Give the location of every parasitized red blood cell.
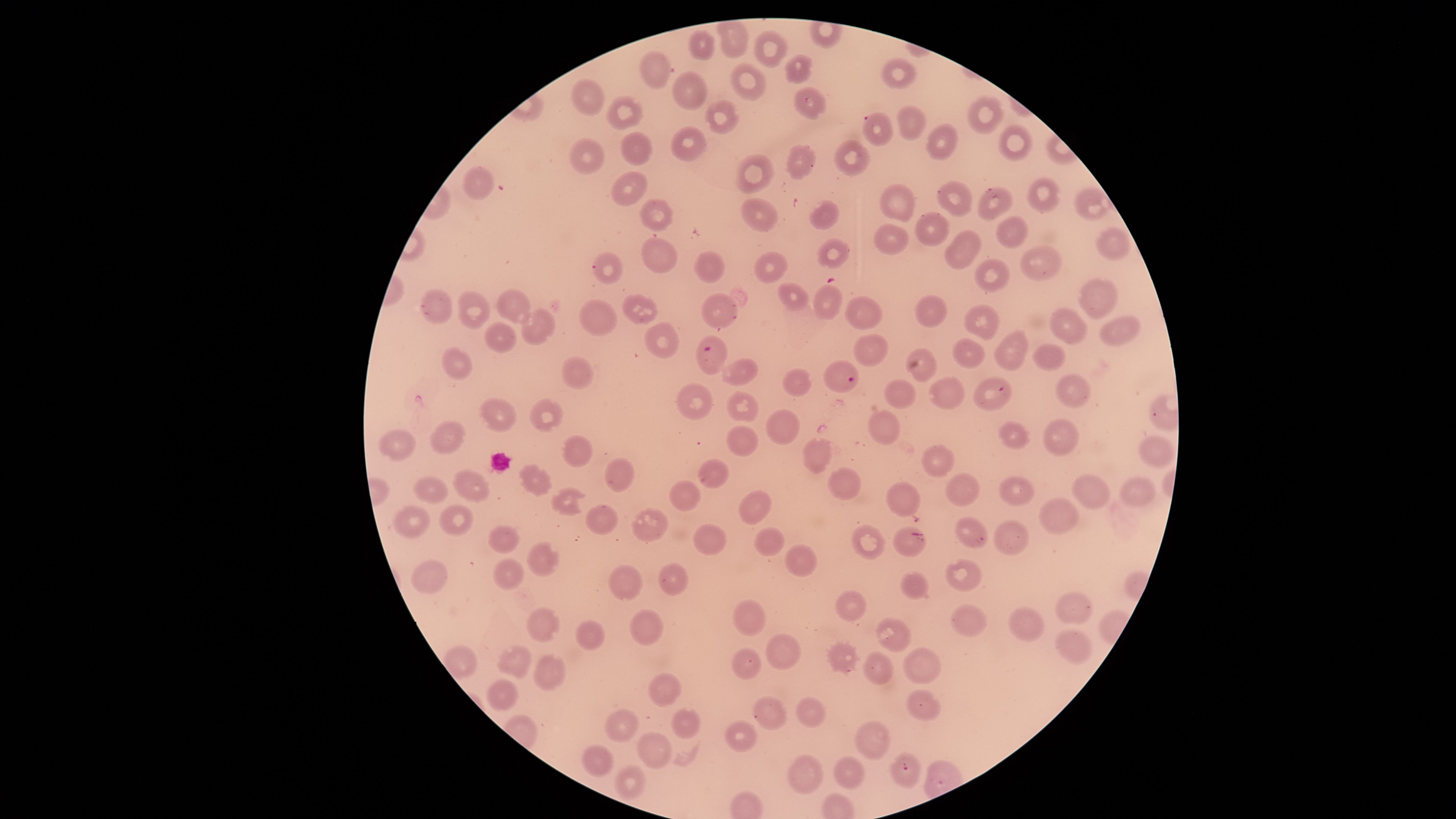
Approximate bounding boxes as (left, top, right, bottom) in pixels.
Parasitized red blood cells: (695, 335, 727, 375), (823, 360, 859, 393).

Approximate bounding boxes as (left, top, right, bottom) in pixels. Uninfected red blood cells: (718, 20, 749, 58), (688, 29, 715, 60), (754, 29, 787, 68), (640, 50, 670, 90), (784, 53, 813, 84), (880, 58, 917, 89), (730, 62, 766, 100), (672, 70, 705, 110), (571, 79, 605, 116), (793, 86, 826, 119), (607, 95, 642, 130), (967, 95, 1004, 134), (706, 99, 739, 135), (895, 105, 926, 140), (863, 111, 893, 145), (928, 123, 959, 160), (999, 124, 1033, 161), (671, 126, 706, 161), (621, 131, 652, 166), (568, 137, 604, 175), (834, 140, 870, 176), (788, 144, 816, 179), (737, 154, 775, 194), (463, 166, 494, 199), (612, 171, 647, 205), (1028, 177, 1059, 213), (938, 180, 972, 216), (880, 184, 915, 224), (978, 187, 1013, 220), (1075, 188, 1111, 221), (739, 197, 779, 232), (639, 198, 673, 232), (810, 200, 839, 229), (915, 211, 949, 246), (996, 216, 1029, 247), (873, 223, 909, 255), (1095, 227, 1130, 260), (944, 229, 983, 269), (641, 237, 678, 273), (817, 238, 851, 268), (1020, 245, 1063, 281), (694, 250, 726, 283), (593, 252, 624, 284), (753, 252, 788, 282), (973, 257, 1010, 291), (1077, 277, 1119, 319), (776, 283, 810, 310), (813, 285, 843, 322), (496, 288, 532, 324), (420, 289, 452, 324), (458, 290, 491, 329), (621, 293, 657, 324), (701, 294, 738, 328), (917, 296, 947, 328), (845, 297, 882, 330), (578, 299, 617, 336), (964, 304, 1001, 340), (521, 308, 554, 345), (1051, 308, 1087, 343), (1100, 314, 1142, 346), (485, 321, 515, 352), (644, 322, 677, 357), (993, 330, 1029, 369), (854, 334, 888, 366), (954, 339, 982, 366), (1033, 344, 1067, 371), (443, 346, 473, 380), (907, 347, 937, 382), (562, 357, 595, 390), (720, 358, 758, 386), (784, 369, 812, 396), (1056, 374, 1091, 408), (973, 376, 1012, 412), (929, 377, 964, 410), (884, 378, 916, 407), (677, 382, 713, 420), (726, 391, 758, 422), (480, 397, 517, 433), (528, 398, 564, 434), (766, 409, 801, 445), (867, 409, 900, 446), (1044, 419, 1078, 456), (430, 420, 467, 455), (998, 420, 1030, 448), (726, 425, 759, 457), (378, 429, 415, 460), (562, 435, 593, 467), (1138, 435, 1176, 467), (803, 437, 833, 473), (921, 444, 954, 478), (604, 457, 634, 492), (698, 458, 729, 488), (520, 463, 552, 496), (827, 467, 862, 500), (454, 470, 490, 501), (946, 473, 981, 507), (1073, 474, 1110, 510), (415, 476, 448, 503), (999, 476, 1036, 506), (1120, 477, 1157, 508), (670, 480, 701, 511), (884, 481, 921, 517), (551, 487, 588, 515), (737, 489, 772, 525), (1039, 497, 1079, 534), (438, 504, 472, 535), (585, 504, 619, 535), (392, 506, 432, 538), (632, 508, 669, 542), (956, 516, 989, 549), (995, 520, 1029, 556), (693, 523, 726, 555), (488, 524, 521, 554), (851, 524, 886, 560), (753, 526, 785, 556), (893, 527, 927, 558), (527, 541, 560, 577), (785, 543, 818, 577), (492, 557, 525, 591), (945, 558, 982, 591), (412, 559, 448, 594), (658, 562, 689, 596), (607, 564, 643, 602), (898, 572, 929, 600), (834, 590, 868, 622), (1056, 590, 1094, 626), (731, 599, 767, 638), (950, 603, 987, 638), (1008, 605, 1044, 642), (527, 607, 560, 642), (628, 608, 664, 646), (875, 617, 911, 652), (574, 620, 606, 650), (1054, 628, 1094, 665), (765, 634, 801, 670), (827, 642, 857, 672), (498, 645, 533, 678), (444, 646, 478, 680), (904, 647, 941, 684), (732, 648, 762, 680), (862, 651, 894, 685), (533, 653, 566, 692), (648, 673, 681, 707), (486, 679, 519, 711), (905, 689, 939, 720), (752, 695, 788, 730), (796, 697, 826, 727), (605, 708, 637, 743), (672, 708, 701, 739), (725, 720, 758, 752), (855, 720, 891, 760), (637, 731, 672, 771), (581, 744, 614, 777), (889, 752, 920, 788), (787, 754, 823, 795), (834, 754, 866, 789), (614, 765, 647, 801). Photographed with a smartphone camera through the microscope eyepiece. Giemsa-stained preparation. Species: Plasmodium falciparum. Thin smear of blood. The visible region is circular. Single field of view. Image is 1456×819 pixels.